Locate every Plasmodium parasite.
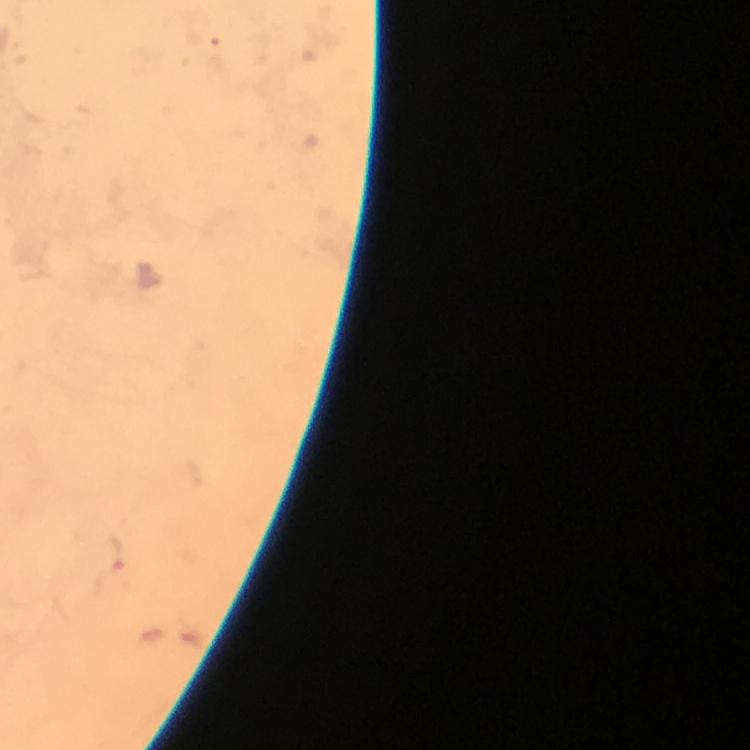
Approximate centers as {x, y} in pixels.
Plasmodium parasites: {116, 556}.

Cropped region of a single field of view. Giemsa stain. Immersion oil applied. Thick blood smear. 100x magnification. From a malaria diagnostic workup. Image is 750×750 pixels. Photographed with a smartphone mounted on the microscope.